Identify the blood parasite species.
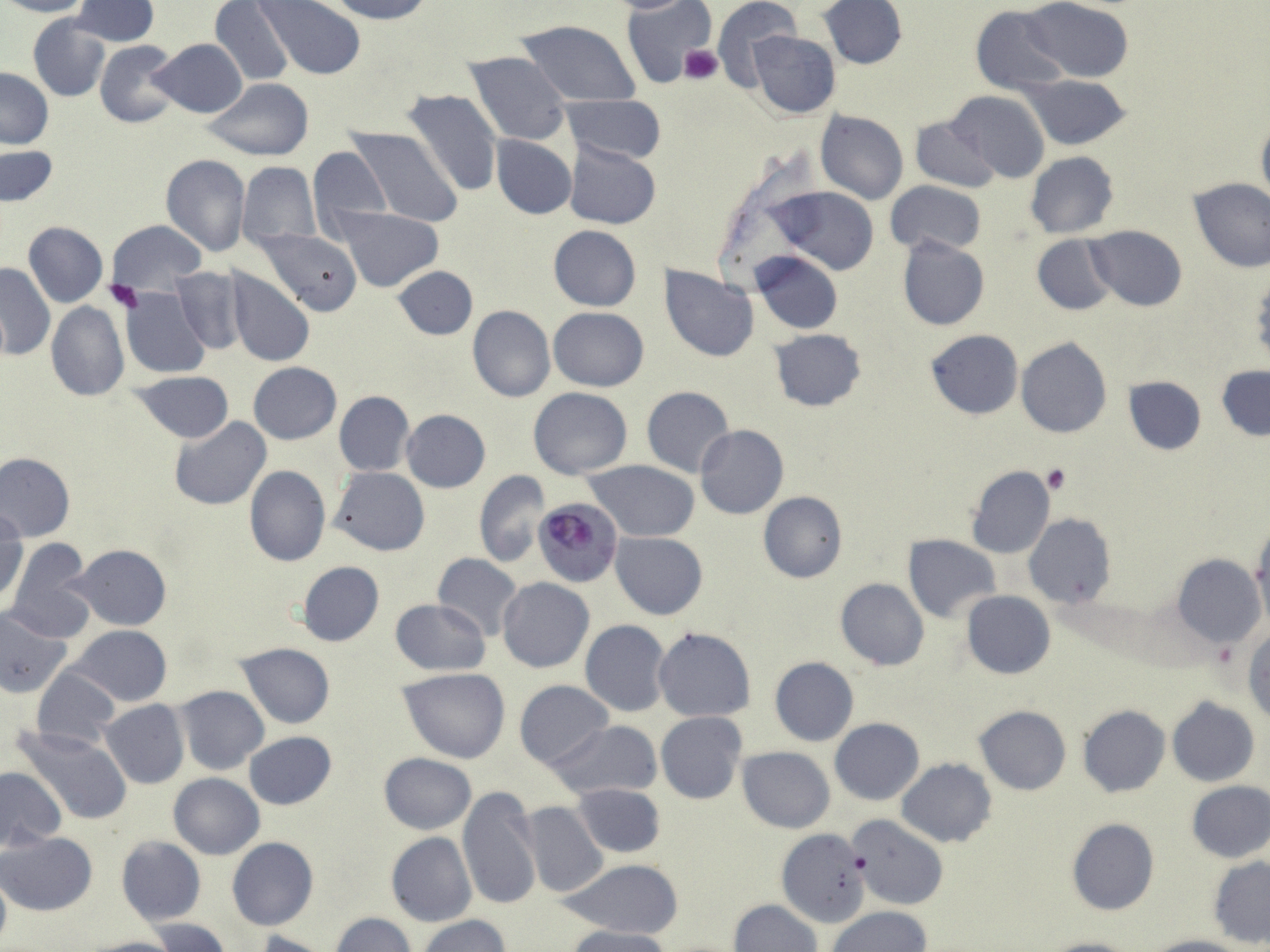

Plasmodium falciparum.

field of view = one of a larger specimen
platelet locations = approximate bounding boxes as (x1, y1, x2, y2) in pixels: (680, 45, 723, 85), (105, 281, 143, 313), (1043, 465, 1071, 493), (1210, 638, 1239, 673)
Plasmodium falciparum-infected red blood cell locations = approximate bounding boxes as (x1, y1, x2, y2) in pixels: (534, 498, 622, 587)
uninfected red blood cell locations = approximate bounding boxes as (x1, y1, x2, y2) in pixels: (0, 0, 89, 17), (72, 0, 159, 47), (253, 0, 367, 79), (326, 0, 433, 24), (601, 0, 706, 13), (710, 0, 801, 87), (210, 1, 295, 87), (621, 1, 718, 86), (819, 1, 906, 69), (1023, 1, 1135, 83), (970, 6, 1070, 97), (29, 16, 110, 101), (514, 19, 642, 107), (748, 30, 841, 119), (150, 39, 247, 118), (95, 41, 183, 127), (465, 51, 571, 146), (1, 68, 53, 148), (1021, 74, 1129, 150), (205, 79, 315, 160), (402, 88, 504, 198), (947, 90, 1049, 183), (561, 95, 666, 163), (816, 110, 907, 205), (910, 116, 999, 193), (1255, 118, 1270, 211), (347, 127, 463, 228), (491, 135, 576, 220), (565, 143, 662, 228), (1, 144, 58, 208), (306, 144, 391, 241), (1025, 151, 1118, 238), (160, 153, 251, 257), (236, 161, 321, 251), (1188, 177, 1270, 273), (885, 181, 985, 257), (772, 186, 878, 275), (337, 208, 442, 291), (107, 220, 205, 294), (23, 222, 107, 307), (547, 225, 641, 312), (1085, 226, 1188, 311), (259, 228, 361, 315), (1032, 235, 1118, 315), (898, 236, 988, 331), (752, 250, 842, 334), (0, 263, 56, 358), (392, 265, 477, 342), (660, 267, 759, 361), (171, 268, 248, 354), (226, 269, 314, 366), (121, 287, 211, 377), (46, 302, 129, 403), (467, 305, 555, 402), (548, 307, 649, 391), (770, 328, 867, 412), (925, 329, 1023, 420), (1016, 337, 1113, 438), (248, 362, 342, 444), (1217, 365, 1270, 441), (133, 371, 234, 444), (1123, 376, 1206, 456), (641, 386, 735, 477), (529, 387, 632, 478), (333, 390, 415, 476), (401, 410, 490, 493), (168, 416, 271, 511), (695, 425, 788, 519), (0, 452, 75, 541), (584, 459, 701, 543), (965, 464, 1055, 559), (245, 465, 331, 567), (329, 467, 429, 555), (473, 469, 551, 567), (757, 492, 847, 583), (1, 510, 26, 604), (1024, 514, 1115, 608), (1249, 524, 1269, 629), (611, 532, 708, 619), (903, 534, 1001, 624), (7, 539, 93, 640), (70, 545, 172, 630), (433, 554, 524, 641), (1173, 554, 1265, 646), (296, 562, 384, 648), (498, 577, 594, 672), (834, 578, 928, 671), (961, 591, 1057, 678), (388, 597, 492, 676), (0, 606, 73, 698), (580, 620, 670, 717), (70, 625, 172, 706), (653, 627, 756, 722), (1244, 627, 1270, 724), (237, 643, 334, 728), (769, 657, 859, 746), (31, 667, 121, 751), (397, 668, 511, 764), (514, 681, 614, 771), (172, 686, 270, 774), (1167, 699, 1259, 786), (100, 700, 189, 789), (1078, 705, 1170, 797), (974, 706, 1071, 795), (656, 712, 747, 804), (829, 718, 924, 804), (546, 720, 662, 800), (16, 727, 133, 825), (243, 731, 337, 810), (737, 747, 835, 833), (378, 752, 476, 833), (896, 758, 997, 847), (0, 766, 67, 851), (168, 773, 265, 859), (1186, 781, 1270, 861), (572, 783, 666, 859), (458, 784, 542, 913), (520, 802, 608, 899), (848, 816, 948, 912), (1067, 819, 1159, 916), (775, 831, 869, 929), (1, 832, 97, 915), (385, 833, 478, 927), (116, 835, 205, 925), (226, 838, 319, 931), (1208, 856, 1270, 948), (561, 859, 683, 939), (0, 872, 11, 948), (727, 899, 821, 952), (829, 906, 930, 952), (331, 913, 415, 952), (419, 915, 511, 952), (148, 918, 232, 951), (566, 926, 676, 952), (254, 930, 331, 952), (1144, 935, 1250, 952), (82, 936, 182, 952), (1038, 936, 1139, 952)
stain = May-Grünwald-Giemsa
modality = light microscopy
magnification = 1000x
preparation = thin blood film
image size = 1270×952 pixels